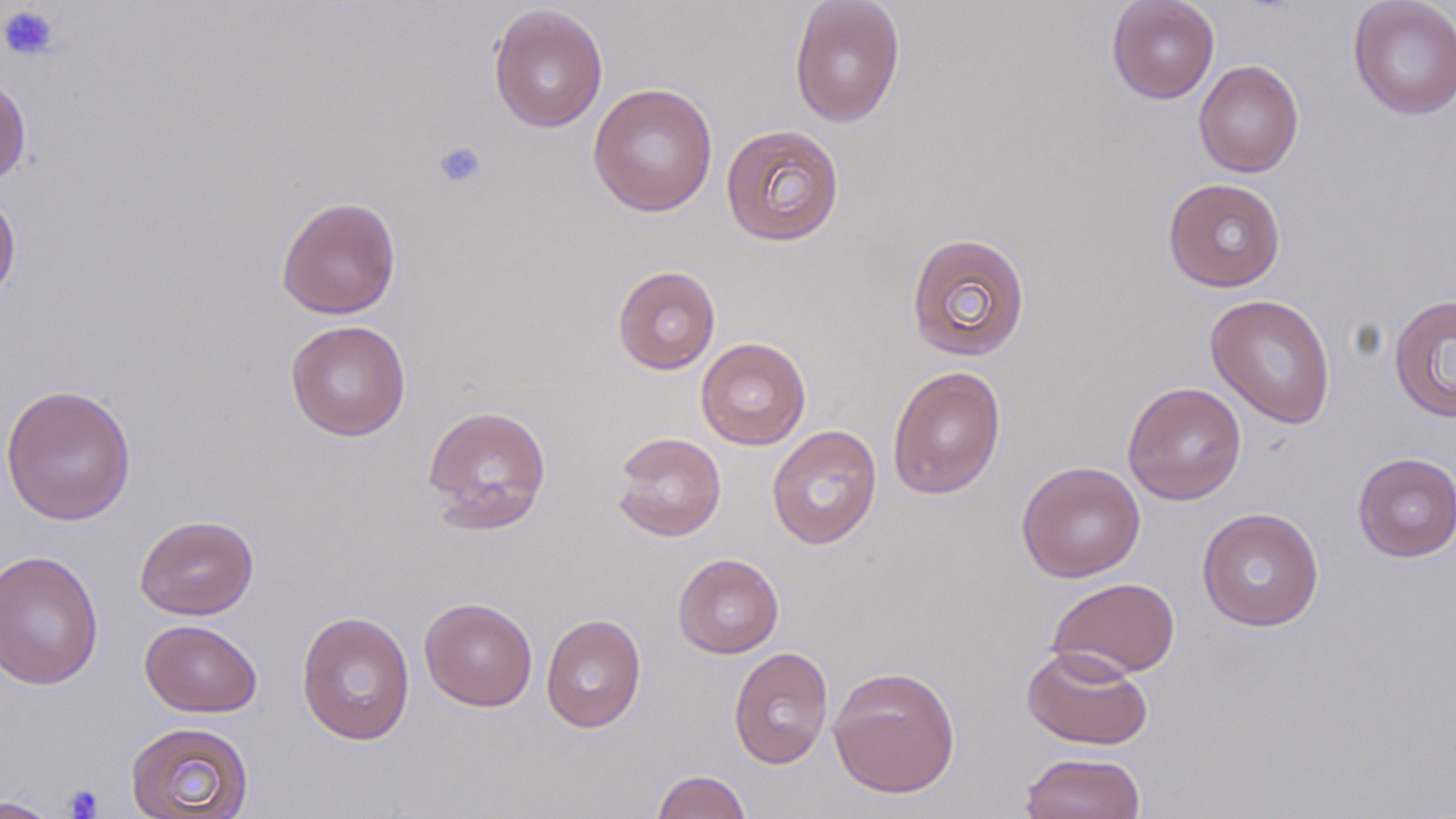
Summary:
  - Coordinate format: approximate bounding boxes as (x1,y1)-(x2,y2) corner pairs in pixels
  - Uninfected red blood cell locations: (788,0)-(906,128), (1106,0)-(1220,104), (1348,0)-(1456,120), (488,4)-(608,133), (1194,59)-(1304,178), (0,75)-(31,186), (588,82)-(718,217), (720,124)-(845,247), (1163,178)-(1286,292), (0,186)-(21,307), (276,195)-(402,320), (906,232)-(1031,362), (612,265)-(721,374), (1205,293)-(1337,429), (1388,293)-(1456,423), (285,320)-(411,441), (696,337)-(811,450), (887,366)-(1006,499), (1122,381)-(1247,506), (0,383)-(137,526), (422,404)-(552,532), (767,424)-(883,550), (612,432)-(727,542), (1352,452)-(1456,562), (1016,460)-(1146,582), (1196,507)-(1325,631), (135,515)-(259,620), (0,550)-(103,690), (672,553)-(784,658), (1047,576)-(1180,679), (419,596)-(537,711), (296,610)-(415,746), (540,613)-(646,733), (140,619)-(262,717), (1022,645)-(1153,751), (728,646)-(833,769), (828,665)-(961,799), (125,721)-(254,818), (1021,751)-(1146,818), (651,769)-(752,819), (0,796)-(62,819)
  - Platelet locations: (0,5)-(60,61), (433,140)-(487,188), (64,784)-(104,818)
  - Slide-level diagnosis: no evidence of blood parasites
  - Modality: optical microscopy
  - Image size: 1456×819 pixels
  - Preparation: thin blood smear
  - Stain: May-Grünwald-Giemsa
  - Magnification: 1000x
  - Field of view: one of a larger specimen